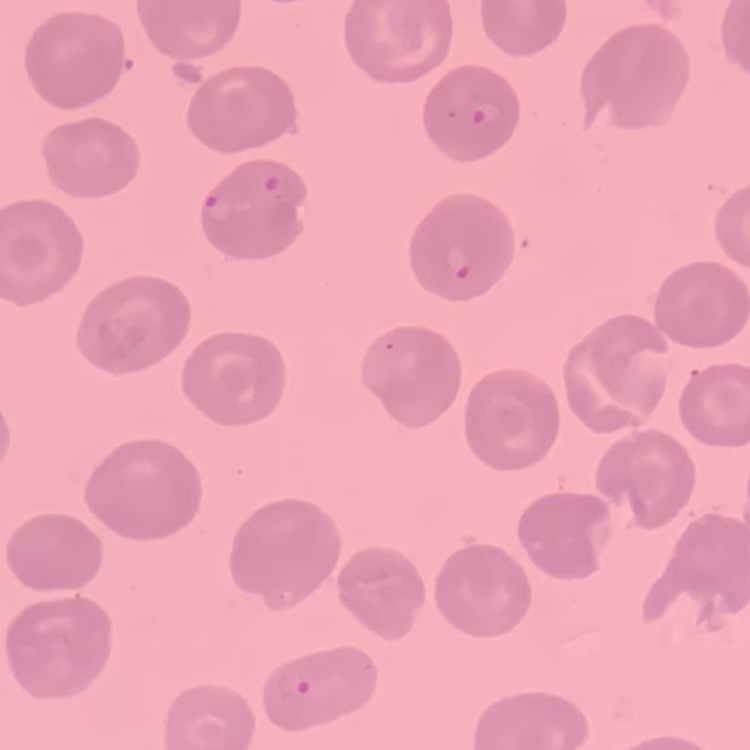

The erythrocytes exhibit no rouleaux formation. Stained with either Field's or Giemsa. One tile cut from a larger photomicrograph. Thin blood film.